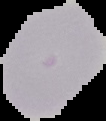

malaria_status: uninfected
image_size: 106×121 pixels
preparation: thin blood film
image_type: cell region segmented out of the field of view; surrounding area masked to black